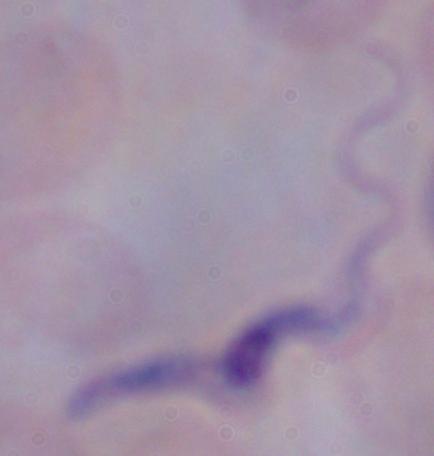
Photomicrograph. A trypanosome is shown. 1000x magnification.